Mark where platelets are.
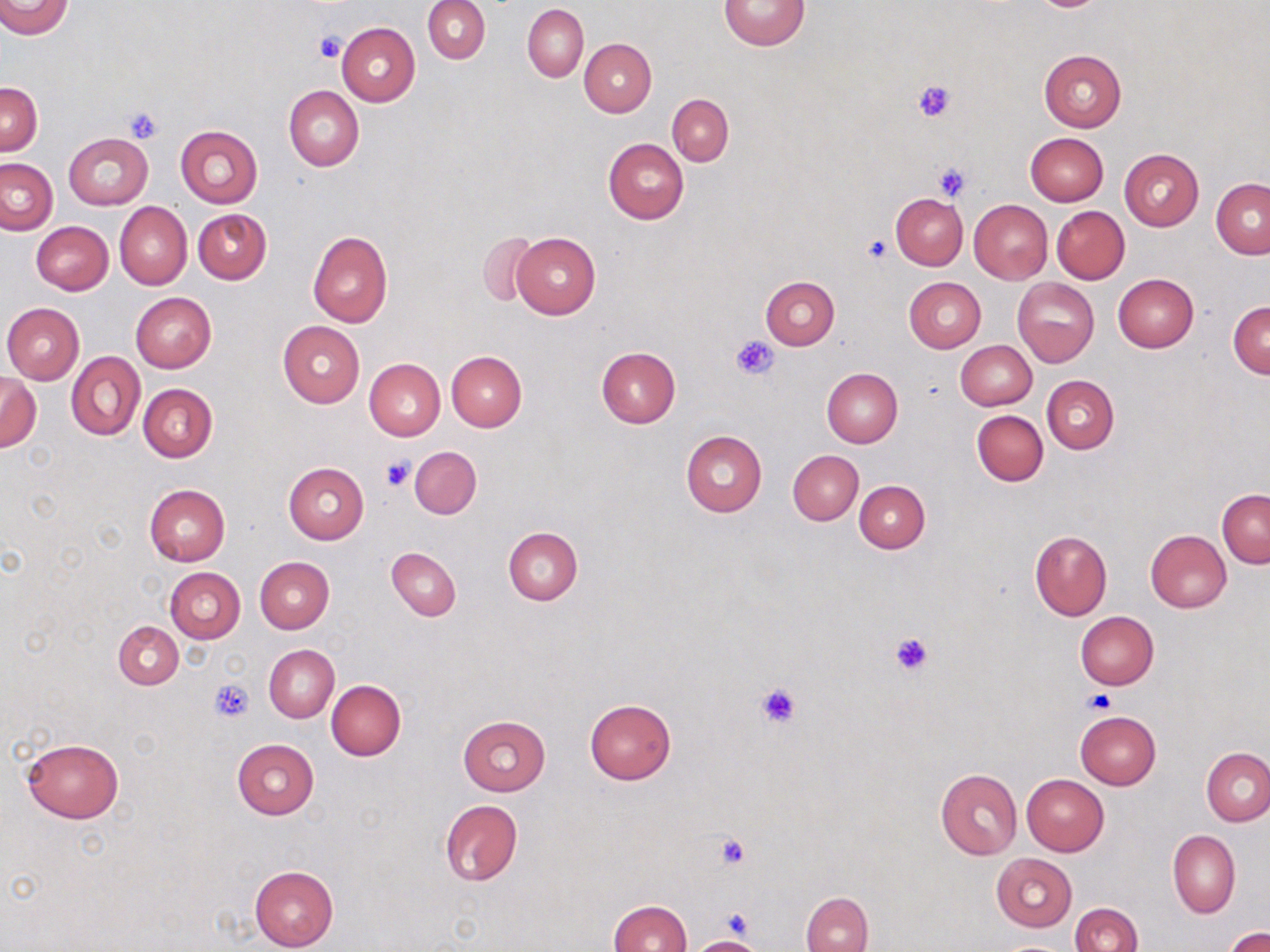

Approximate bounding boxes as named x1/y1/x2/y2 corners in pixels.
Platelets: (x1=314, y1=32, x2=346, y2=63), (x1=911, y1=79, x2=957, y2=122), (x1=122, y1=104, x2=164, y2=142), (x1=932, y1=162, x2=972, y2=200), (x1=862, y1=236, x2=891, y2=264), (x1=732, y1=334, x2=780, y2=380), (x1=380, y1=455, x2=414, y2=491), (x1=890, y1=632, x2=934, y2=676), (x1=209, y1=681, x2=253, y2=721), (x1=756, y1=682, x2=802, y2=728), (x1=1084, y1=690, x2=1115, y2=715), (x1=715, y1=834, x2=751, y2=871), (x1=724, y1=907, x2=752, y2=940).

Uninfected red blood cell locations: (x1=2, y1=0, x2=72, y2=38), (x1=424, y1=0, x2=490, y2=63), (x1=720, y1=0, x2=810, y2=50), (x1=522, y1=4, x2=589, y2=81), (x1=336, y1=22, x2=420, y2=106), (x1=579, y1=38, x2=656, y2=117), (x1=1040, y1=50, x2=1127, y2=131), (x1=1, y1=83, x2=42, y2=155), (x1=284, y1=85, x2=364, y2=172), (x1=667, y1=94, x2=733, y2=166), (x1=174, y1=125, x2=263, y2=208), (x1=63, y1=132, x2=153, y2=210), (x1=1026, y1=133, x2=1108, y2=206), (x1=604, y1=139, x2=688, y2=223), (x1=1120, y1=149, x2=1204, y2=230), (x1=1, y1=159, x2=57, y2=234), (x1=1211, y1=178, x2=1270, y2=258), (x1=891, y1=193, x2=968, y2=270), (x1=969, y1=200, x2=1052, y2=284), (x1=115, y1=202, x2=192, y2=289), (x1=1052, y1=206, x2=1129, y2=283), (x1=194, y1=209, x2=271, y2=284), (x1=32, y1=221, x2=113, y2=295), (x1=308, y1=232, x2=392, y2=327), (x1=477, y1=232, x2=539, y2=307), (x1=510, y1=233, x2=600, y2=319), (x1=1112, y1=274, x2=1198, y2=353), (x1=760, y1=275, x2=839, y2=349), (x1=904, y1=276, x2=986, y2=352), (x1=1013, y1=277, x2=1099, y2=366), (x1=131, y1=292, x2=216, y2=372), (x1=1228, y1=301, x2=1270, y2=378), (x1=2, y1=303, x2=84, y2=384), (x1=278, y1=321, x2=364, y2=406), (x1=955, y1=340, x2=1036, y2=411), (x1=596, y1=347, x2=680, y2=428), (x1=66, y1=351, x2=145, y2=441), (x1=446, y1=351, x2=527, y2=431), (x1=364, y1=358, x2=445, y2=440), (x1=821, y1=367, x2=902, y2=447), (x1=0, y1=372, x2=41, y2=451), (x1=1043, y1=376, x2=1119, y2=454), (x1=139, y1=384, x2=217, y2=462), (x1=971, y1=409, x2=1048, y2=486), (x1=681, y1=430, x2=767, y2=516), (x1=410, y1=446, x2=482, y2=519), (x1=788, y1=450, x2=863, y2=524), (x1=283, y1=462, x2=369, y2=543), (x1=854, y1=480, x2=930, y2=553), (x1=145, y1=485, x2=230, y2=566), (x1=1218, y1=489, x2=1269, y2=569), (x1=504, y1=527, x2=583, y2=604), (x1=1030, y1=530, x2=1111, y2=621), (x1=1146, y1=530, x2=1232, y2=612), (x1=386, y1=547, x2=461, y2=620), (x1=254, y1=556, x2=334, y2=633), (x1=165, y1=567, x2=245, y2=642), (x1=1075, y1=611, x2=1159, y2=690), (x1=114, y1=622, x2=183, y2=689), (x1=264, y1=644, x2=339, y2=723), (x1=326, y1=681, x2=405, y2=760), (x1=584, y1=698, x2=677, y2=784), (x1=1074, y1=711, x2=1160, y2=789), (x1=457, y1=715, x2=551, y2=795), (x1=20, y1=738, x2=125, y2=824), (x1=232, y1=738, x2=318, y2=818), (x1=1201, y1=747, x2=1270, y2=826), (x1=935, y1=769, x2=1022, y2=859), (x1=1021, y1=774, x2=1109, y2=855), (x1=439, y1=799, x2=522, y2=886), (x1=1167, y1=830, x2=1240, y2=919), (x1=992, y1=853, x2=1076, y2=931), (x1=249, y1=865, x2=338, y2=951), (x1=801, y1=891, x2=872, y2=952), (x1=607, y1=900, x2=692, y2=952), (x1=1070, y1=903, x2=1142, y2=952), (x1=1224, y1=927, x2=1270, y2=952), (x1=689, y1=936, x2=766, y2=951), (x1=997, y1=941, x2=1068, y2=952). Slide-level diagnosis: negative for blood parasites. Light microscopy. Thin blood film. One field of a larger specimen. Image is 1270×952 pixels. May-Grünwald-Giemsa stain. 1000x magnification.